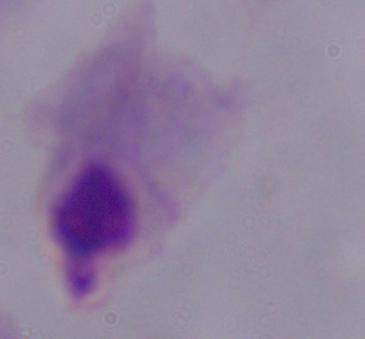 Micrograph. 1000x magnification. A trichomonad is shown.